Describe the morphology of the red blood cells.
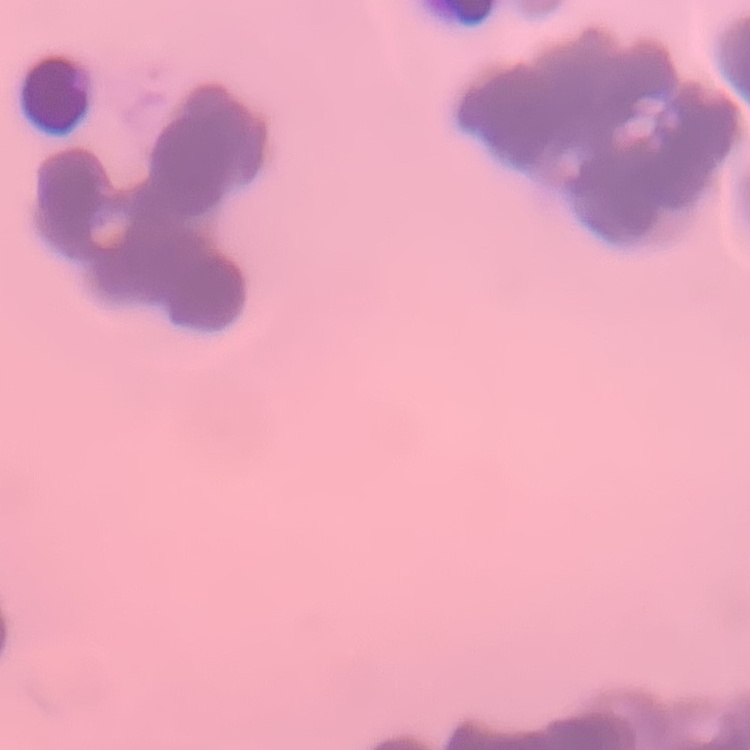
They show rouleaux formation.

stain: Field's or Giemsa
image_type: one tile cut from a larger photomicrograph
preparation: thin blood smear